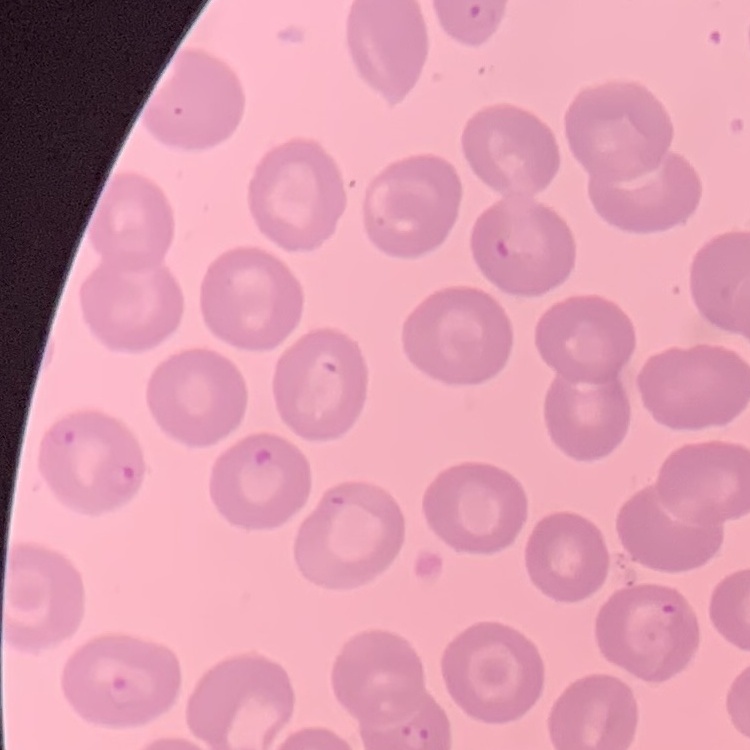

red_blood_cell_morphology: no rouleaux formation
image_type: square crop of a larger photomicrograph
stain: Field's or Giemsa
preparation: thin peripheral smear